Classify this cell by malaria status.
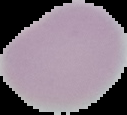
It is uninfected.

{
  "preparation": "thin blood smear",
  "image_type": "segmented cell region with the area outside set to black",
  "image_size": "127×115 pixels"
}